Comment on the morphology of the erythrocytes.
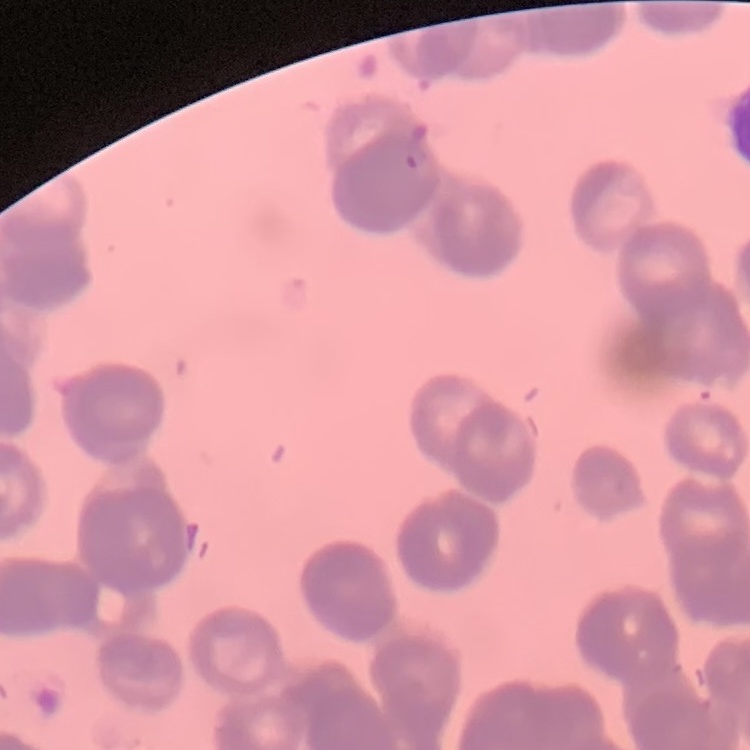
They show rouleaux formation.

Stained with either Field's or Giemsa. Thin blood smear. Square crop of a larger photomicrograph.